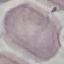

Malaria status: uninfected. Photographed with a smartphone camera at the microscope eyepiece. Giemsa stain. Automatically extracted cell patch, resized to 64 × 64 pixels. Thin smear of blood.